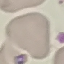
{
  "malaria_status": "uninfected",
  "image_type": "cell patch, automatically extracted from a larger field of view and resized to 64 × 64 pixels",
  "stain": "Giemsa",
  "preparation": "thin blood film",
  "capture": "smartphone through the microscope eyepiece"
}